Classify this cell by malaria status.
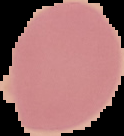

It is uninfected.

From a thin blood film. The area outside the segmented cell region is set to black. Image is 124×136 pixels.